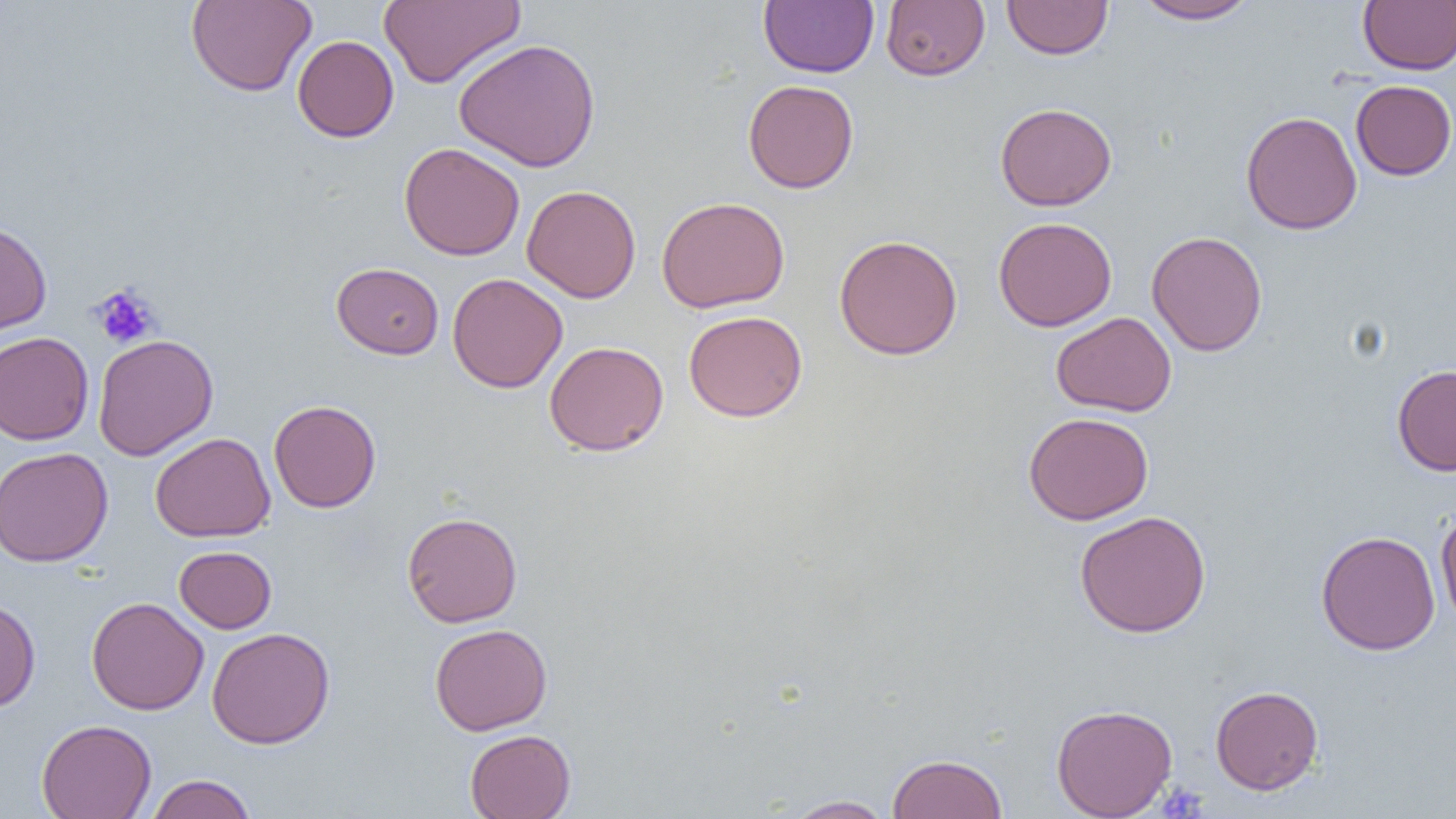 Approximate bounding boxes as [x1, y1, x2, y2] in pixels. Uninfected red blood cell locations: [185, 0, 316, 97], [379, 0, 526, 88], [881, 0, 989, 81], [1358, 0, 1456, 75], [759, 1, 879, 77], [1002, 1, 1113, 60], [1133, 1, 1260, 24], [292, 35, 399, 142], [453, 38, 601, 172], [743, 79, 859, 193], [1350, 79, 1456, 180], [995, 102, 1117, 211], [1240, 111, 1362, 235], [398, 142, 525, 261], [521, 185, 641, 303], [656, 196, 790, 313], [993, 216, 1117, 331], [0, 221, 53, 335], [1146, 231, 1268, 356], [834, 234, 963, 360], [331, 262, 444, 359], [447, 273, 567, 393], [683, 310, 808, 423], [1051, 311, 1177, 417], [0, 331, 94, 445], [93, 333, 218, 460], [543, 340, 669, 456], [1392, 364, 1456, 476], [269, 399, 381, 513], [1024, 412, 1154, 525], [150, 432, 276, 542], [0, 446, 113, 567], [1436, 506, 1456, 631], [1074, 510, 1211, 637], [402, 512, 523, 628], [1315, 530, 1441, 655], [174, 545, 277, 633], [0, 596, 41, 713], [86, 596, 209, 715], [429, 623, 552, 736], [207, 626, 335, 749], [1210, 685, 1323, 795], [1051, 703, 1178, 818], [36, 718, 156, 819], [464, 729, 576, 819], [887, 752, 1008, 818], [145, 774, 257, 819], [784, 795, 895, 818]. Platelet locations: [92, 285, 158, 349], [1156, 781, 1209, 818]. Slide-level diagnosis: no evidence of blood parasites. Image is 1456×819 pixels. Thin blood film. Single field of view. Light microscopy. Captured at 1000x magnification.